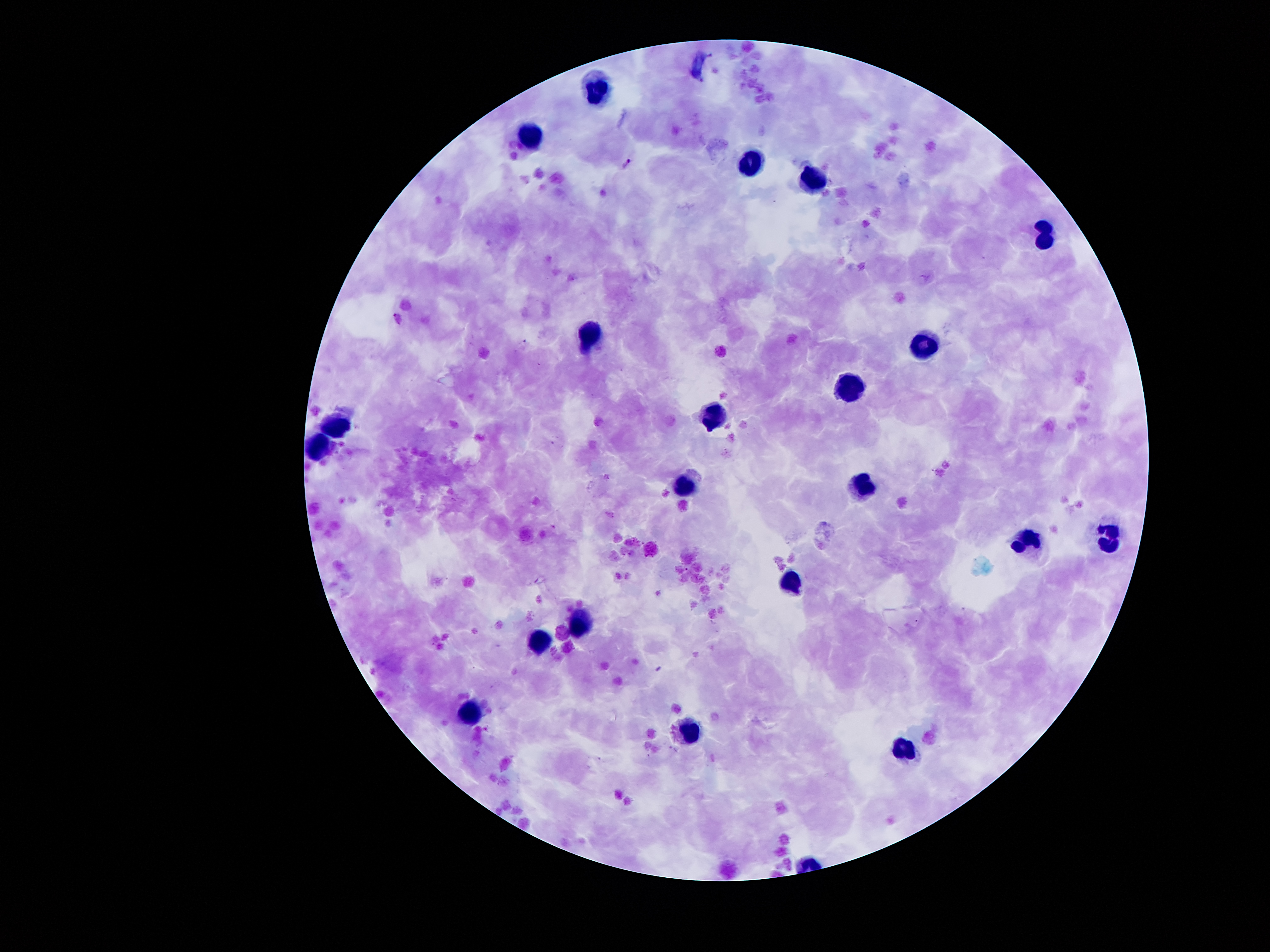
Approximate centers as [x, y] in pixels. Plasmodium parasite locations: [628, 164]. Leukocyte locations: [600, 88], [529, 134], [750, 162], [811, 181], [1044, 235], [593, 333], [921, 340], [848, 387], [714, 419], [335, 423], [319, 443], [686, 483], [864, 484], [1110, 532], [1029, 534], [790, 578], [582, 621], [537, 641], [469, 709], [690, 725], [902, 752]. Giemsa-stained preparation. Thick blood smear. 100x magnification. Patient malaria status: infected with Plasmodium falciparum. Photographed through the microscope eyepiece with a smartphone camera. Image is 1270×952 pixels. One field from this slide.